Report the malaria status of this cell.
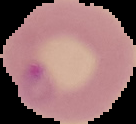
Parasitized.

From a thin blood film. Image is 136×124 pixels. Cell region segmented out of the field of view; the surrounding area is masked to black.